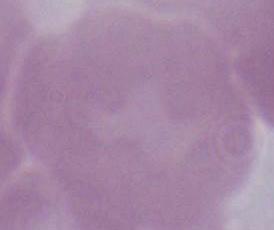

magnification = 1000x
identification = erythrocyte
modality = photomicrograph